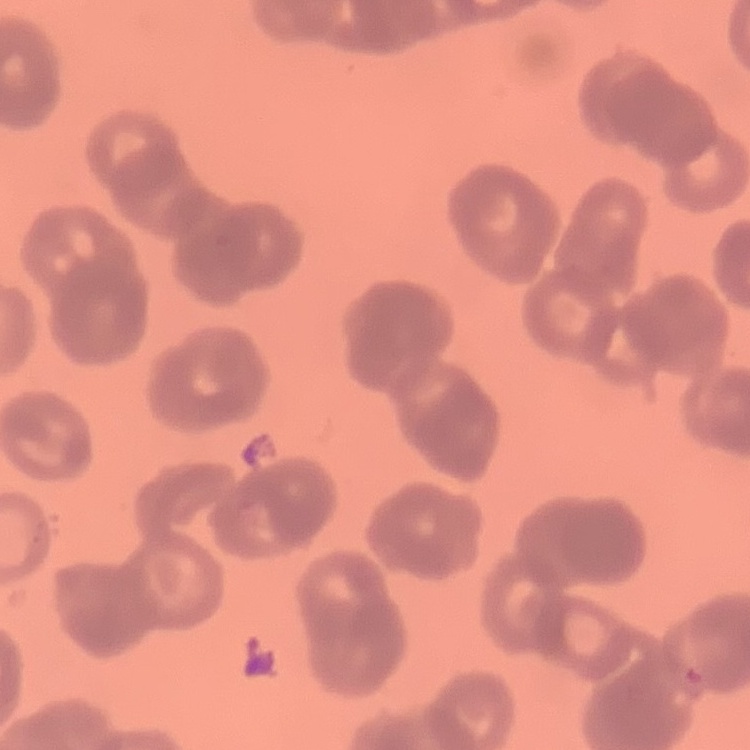 The erythrocytes show rouleaux formation. Thin peripheral smear. Stained with either Field's or Giemsa. Square crop of a larger photomicrograph.